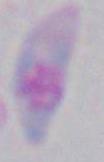
Summary:
  - Identification: Toxoplasma gondii
  - Magnification: 1000x
  - Modality: micrograph